Classify this cell by malaria status.
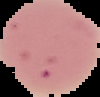

Uninfected.

image type = segmented cell region with the area outside set to black
preparation = thin blood smear
image size = 100×97 pixels